Point out each Plasmodium parasite.
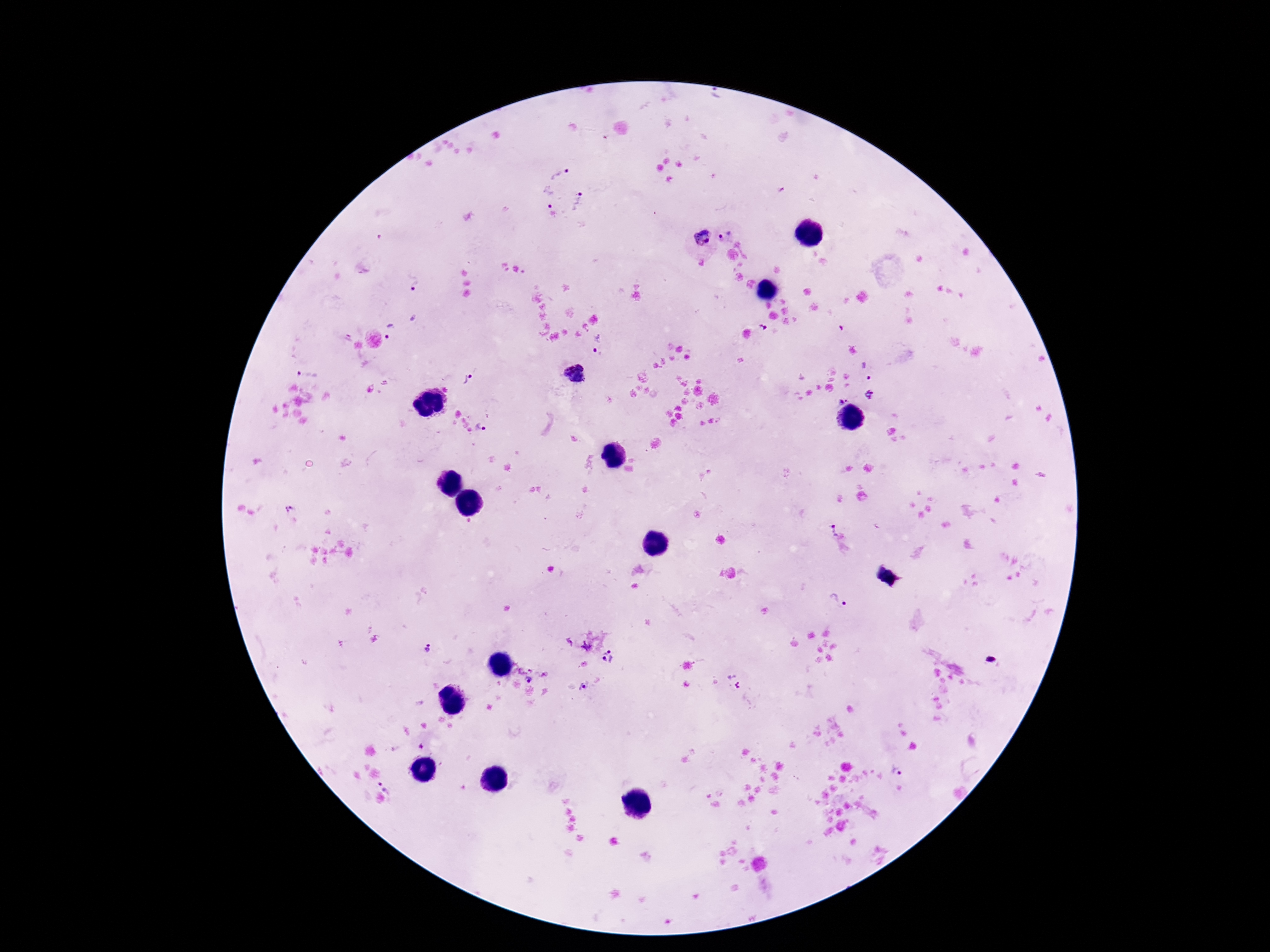
Approximate centers as [x, y] in pixels.
Plasmodium parasites: [716, 96], [561, 171], [547, 198], [580, 202], [727, 233], [702, 238], [414, 282], [392, 332], [346, 337], [598, 344], [867, 368], [308, 372], [467, 378], [871, 395], [842, 399], [482, 427], [286, 507], [830, 529], [839, 599], [588, 644], [427, 648], [608, 656], [534, 670], [528, 678], [734, 681], [585, 687], [899, 771], [389, 787].

100x magnification. Single field of view. Photographed through the microscope eyepiece with a smartphone camera. Image is 1270×952 pixels. Giemsa-stained preparation. Thick peripheral-blood smear. Patient malaria status: infected.